Comment on the morphology of the red blood cells.
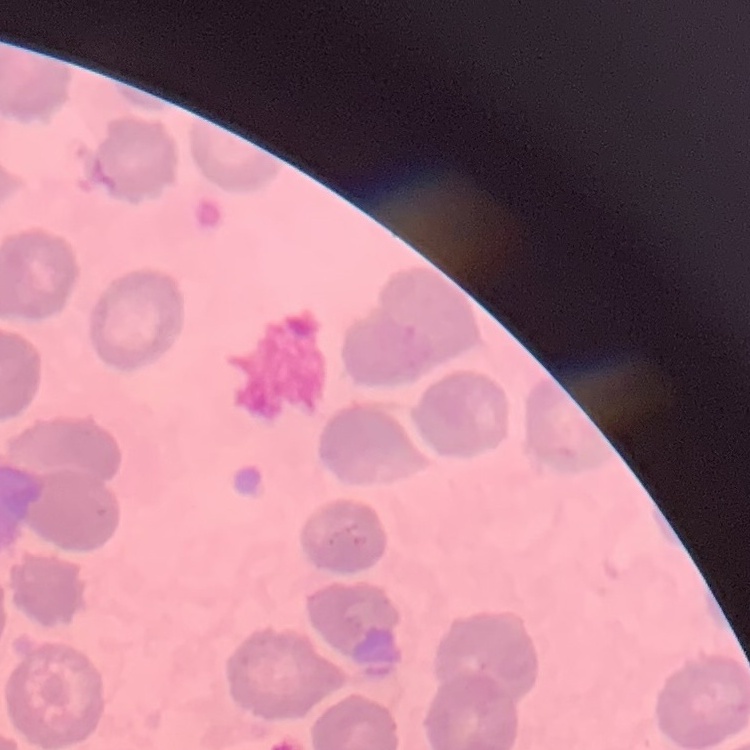

They show no rouleaux formation.

stain = Field's or Giemsa
preparation = thin blood smear
image type = square crop of a larger photomicrograph